Identify the parasite.
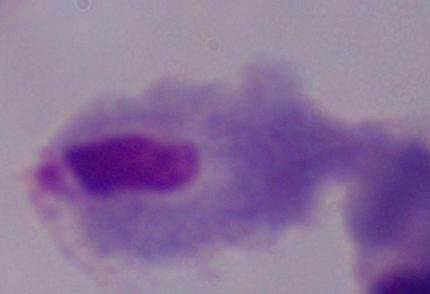
This is a trichomonad.

modality = photomicrograph
magnification = 1000x